Locate every Plasmodium ovale-infected red blood cell.
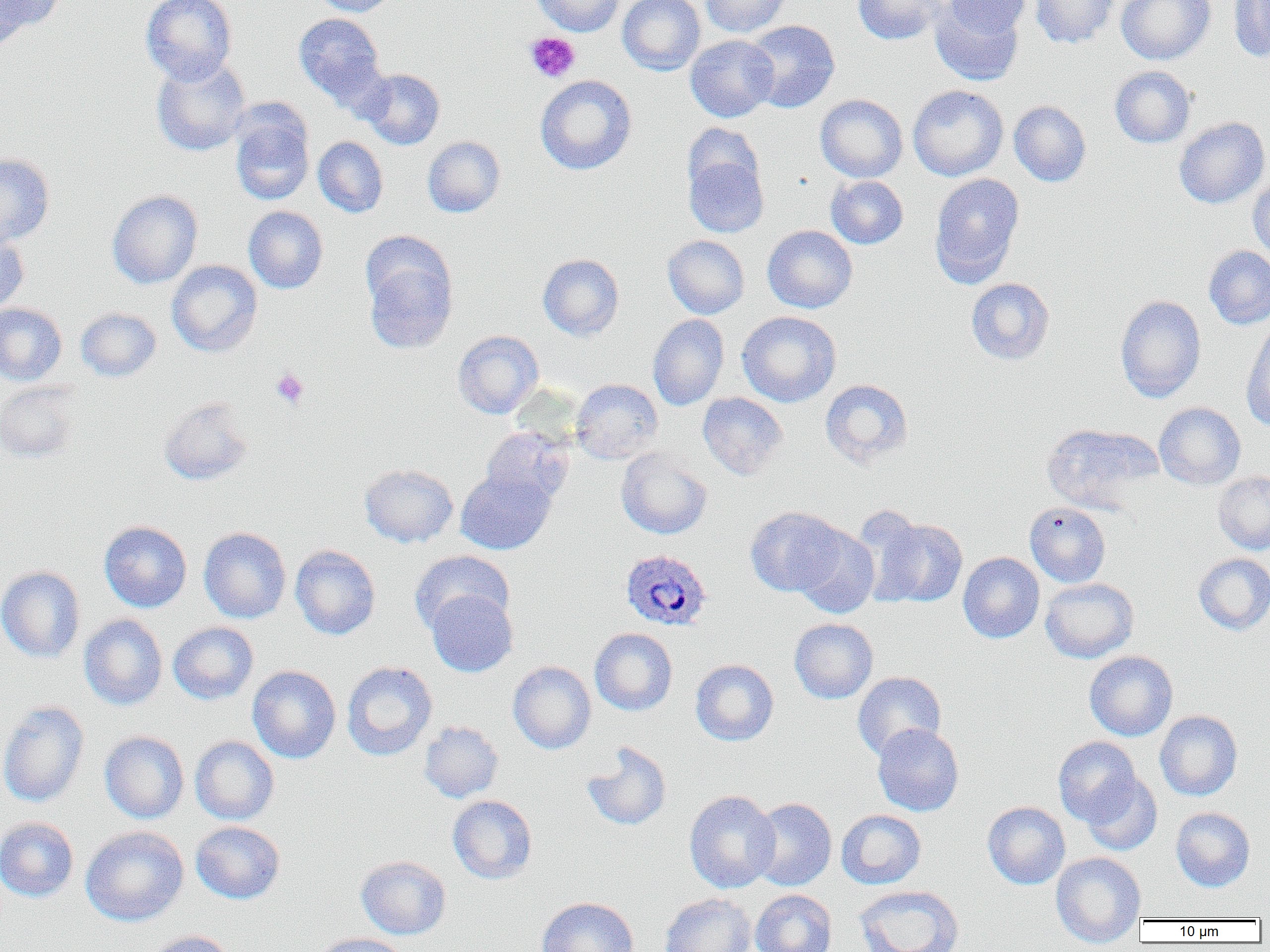
Approximate bounding boxes as named x1/y1/x2/y2 corners in pixels.
Plasmodium ovale-infected red blood cells: (x1=620, y1=549, x2=712, y2=631).

slide_level_diagnosis: Plasmodium ovale
magnification: 1000x
preparation: thin blood film
field_of_view: single
platelet_locations: 'approximate bounding boxes as named x1/y1/x2/y2 corners in pixels: (x1=524, y1=31, x2=581, y2=83), (x1=271, y1=368, x2=309, y2=409)'
modality: optical microscopy
image_size: 1270×952 pixels
uninfected_red_blood_cell_locations: 'approximate bounding boxes as named x1/y1/x2/y2 corners in pixels: (x1=1, y1=0, x2=64, y2=36), (x1=141, y1=0, x2=237, y2=85), (x1=308, y1=0, x2=400, y2=16), (x1=531, y1=0, x2=625, y2=36), (x1=617, y1=0, x2=705, y2=75), (x1=700, y1=0, x2=793, y2=38), (x1=852, y1=0, x2=947, y2=45), (x1=942, y1=0, x2=1032, y2=38), (x1=1030, y1=0, x2=1118, y2=48), (x1=1116, y1=0, x2=1215, y2=65), (x1=1228, y1=1, x2=1270, y2=61), (x1=930, y1=2, x2=1024, y2=86), (x1=293, y1=13, x2=388, y2=108), (x1=743, y1=20, x2=840, y2=113), (x1=685, y1=35, x2=779, y2=122), (x1=151, y1=56, x2=251, y2=156), (x1=1110, y1=66, x2=1196, y2=148), (x1=358, y1=68, x2=444, y2=150), (x1=535, y1=75, x2=637, y2=175), (x1=908, y1=85, x2=1008, y2=181), (x1=815, y1=94, x2=908, y2=182), (x1=1009, y1=100, x2=1091, y2=187), (x1=229, y1=104, x2=315, y2=205), (x1=1174, y1=117, x2=1270, y2=208), (x1=682, y1=122, x2=765, y2=199), (x1=313, y1=136, x2=388, y2=218), (x1=423, y1=136, x2=505, y2=218), (x1=683, y1=152, x2=768, y2=238), (x1=0, y1=153, x2=55, y2=247), (x1=929, y1=173, x2=1025, y2=288), (x1=826, y1=176, x2=908, y2=249), (x1=1248, y1=177, x2=1270, y2=264), (x1=107, y1=190, x2=203, y2=289), (x1=243, y1=206, x2=328, y2=294), (x1=762, y1=225, x2=857, y2=313), (x1=0, y1=228, x2=29, y2=316), (x1=662, y1=235, x2=749, y2=319), (x1=362, y1=241, x2=458, y2=355), (x1=1203, y1=246, x2=1270, y2=329), (x1=538, y1=253, x2=624, y2=341), (x1=166, y1=260, x2=263, y2=357), (x1=966, y1=277, x2=1055, y2=365), (x1=1115, y1=295, x2=1206, y2=403), (x1=0, y1=302, x2=67, y2=386), (x1=75, y1=307, x2=161, y2=382), (x1=736, y1=311, x2=841, y2=407), (x1=648, y1=314, x2=729, y2=411), (x1=1241, y1=321, x2=1270, y2=431), (x1=452, y1=330, x2=544, y2=418), (x1=570, y1=379, x2=663, y2=463), (x1=820, y1=379, x2=914, y2=469), (x1=0, y1=382, x2=81, y2=464), (x1=697, y1=392, x2=788, y2=481), (x1=158, y1=397, x2=255, y2=486), (x1=1154, y1=402, x2=1245, y2=490), (x1=1041, y1=423, x2=1158, y2=514), (x1=480, y1=426, x2=573, y2=506), (x1=616, y1=448, x2=712, y2=539), (x1=359, y1=463, x2=458, y2=547), (x1=455, y1=468, x2=556, y2=555), (x1=1213, y1=471, x2=1270, y2=554), (x1=1025, y1=502, x2=1111, y2=587), (x1=745, y1=506, x2=846, y2=597), (x1=870, y1=517, x2=968, y2=608), (x1=99, y1=521, x2=192, y2=613), (x1=792, y1=524, x2=880, y2=618), (x1=198, y1=526, x2=291, y2=623), (x1=289, y1=544, x2=381, y2=640), (x1=409, y1=550, x2=515, y2=635), (x1=958, y1=552, x2=1044, y2=643), (x1=1193, y1=553, x2=1270, y2=635), (x1=0, y1=565, x2=86, y2=663), (x1=1040, y1=578, x2=1138, y2=663), (x1=425, y1=589, x2=518, y2=677), (x1=79, y1=614, x2=168, y2=711), (x1=789, y1=618, x2=878, y2=704), (x1=168, y1=622, x2=258, y2=704), (x1=590, y1=628, x2=677, y2=716), (x1=1084, y1=651, x2=1178, y2=741), (x1=690, y1=659, x2=779, y2=746), (x1=341, y1=661, x2=438, y2=760), (x1=508, y1=661, x2=596, y2=754), (x1=247, y1=666, x2=341, y2=763), (x1=852, y1=671, x2=946, y2=760), (x1=0, y1=700, x2=89, y2=807), (x1=1155, y1=710, x2=1242, y2=801), (x1=419, y1=721, x2=503, y2=803), (x1=872, y1=724, x2=964, y2=816), (x1=99, y1=731, x2=189, y2=823), (x1=189, y1=736, x2=279, y2=825), (x1=1053, y1=736, x2=1142, y2=825), (x1=581, y1=741, x2=671, y2=831), (x1=1082, y1=772, x2=1163, y2=855), (x1=684, y1=790, x2=780, y2=893), (x1=447, y1=795, x2=537, y2=884), (x1=748, y1=798, x2=837, y2=891), (x1=982, y1=801, x2=1070, y2=889), (x1=1170, y1=807, x2=1255, y2=892), (x1=837, y1=810, x2=926, y2=889), (x1=0, y1=817, x2=79, y2=902), (x1=190, y1=821, x2=285, y2=904), (x1=80, y1=826, x2=189, y2=926), (x1=1051, y1=852, x2=1145, y2=948), (x1=356, y1=855, x2=451, y2=939), (x1=853, y1=884, x2=964, y2=952), (x1=751, y1=889, x2=837, y2=952), (x1=659, y1=893, x2=756, y2=952), (x1=536, y1=896, x2=639, y2=952), (x1=143, y1=930, x2=238, y2=952), (x1=311, y1=933, x2=411, y2=952)'